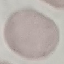
malaria_status: uninfected
preparation: thin blood smear
image_type: cell patch, automatically extracted from a larger field of view and resized to 64 × 64 pixels
capture: smartphone camera at the microscope eyepiece
stain: Giemsa